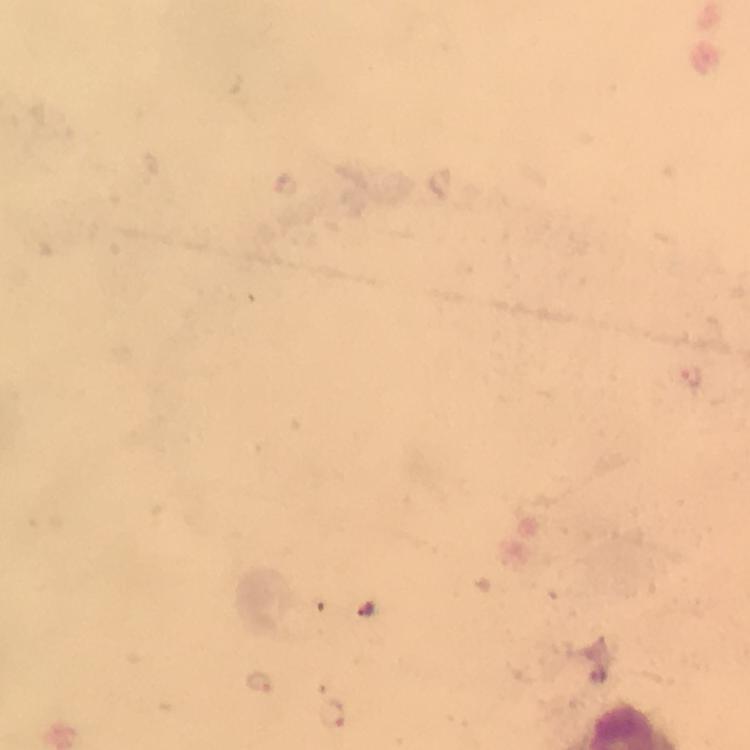
Approximate centers as {x, y} in pixels.
Summary:
  - Malaria parasite locations: {260, 683}
  - Preparation: thick blood film
  - Image size: 750×750 pixels
  - Capture: smartphone mounted on the microscope
  - Context: from a diagnostic examination for malaria
  - Stain: Giemsa
  - Magnification: 100x
  - Immersion oil: used
  - Cropped from: a single field of view